Locate every blood parasite and identify its species.
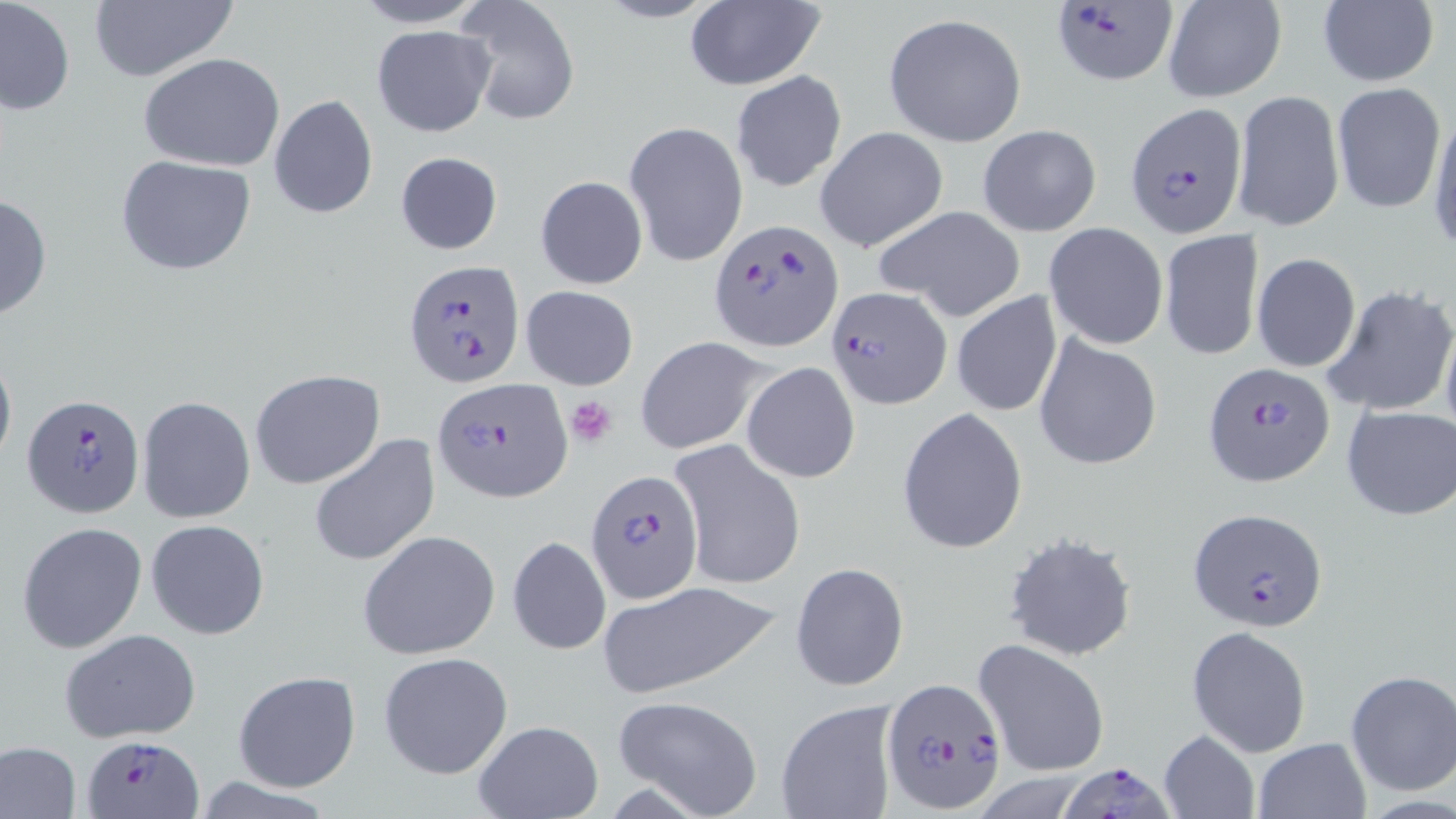

Approximate bounding boxes as named x1/y1/x2/y2 corners in pixels.
Plasmodium falciparum-infected red blood cells: (x1=1049, y1=0, x2=1177, y2=85), (x1=1125, y1=102, x2=1246, y2=235), (x1=711, y1=219, x2=841, y2=353), (x1=405, y1=259, x2=523, y2=389), (x1=826, y1=286, x2=951, y2=410), (x1=1200, y1=363, x2=1334, y2=488), (x1=433, y1=376, x2=571, y2=502), (x1=23, y1=393, x2=144, y2=518), (x1=585, y1=471, x2=703, y2=604), (x1=1188, y1=505, x2=1327, y2=633), (x1=881, y1=676, x2=1008, y2=814), (x1=78, y1=734, x2=207, y2=817), (x1=1057, y1=763, x2=1173, y2=819).
No Plasmodium ovale, Plasmodium malariae, Plasmodium vivax, Babesia divergens, or Trypanosoma brucei observed.

slide-level diagnosis = Plasmodium falciparum
field of view = one of a larger specimen
image size = 1456×819 pixels
stain = May-Grünwald-Giemsa
uninfected red blood cell locations = approximate bounding boxes as named x1/y1/x2/y2 corners in pixels: (x1=1, y1=0, x2=75, y2=116), (x1=347, y1=0, x2=493, y2=28), (x1=590, y1=0, x2=727, y2=24), (x1=1317, y1=0, x2=1439, y2=88), (x1=456, y1=1, x2=580, y2=126), (x1=1161, y1=1, x2=1287, y2=103), (x1=683, y1=2, x2=824, y2=90), (x1=87, y1=3, x2=239, y2=82), (x1=882, y1=13, x2=1027, y2=146), (x1=371, y1=25, x2=496, y2=135), (x1=138, y1=54, x2=285, y2=172), (x1=729, y1=70, x2=848, y2=193), (x1=1332, y1=81, x2=1446, y2=213), (x1=1232, y1=88, x2=1345, y2=232), (x1=268, y1=94, x2=378, y2=220), (x1=1426, y1=108, x2=1456, y2=258), (x1=623, y1=121, x2=748, y2=268), (x1=977, y1=125, x2=1103, y2=236), (x1=814, y1=127, x2=948, y2=252), (x1=394, y1=151, x2=504, y2=255), (x1=114, y1=155, x2=259, y2=277), (x1=534, y1=174, x2=648, y2=289), (x1=0, y1=193, x2=52, y2=321), (x1=873, y1=203, x2=1027, y2=321), (x1=1044, y1=222, x2=1169, y2=350), (x1=1159, y1=231, x2=1263, y2=360), (x1=1251, y1=253, x2=1361, y2=372), (x1=1321, y1=282, x2=1456, y2=417), (x1=520, y1=285, x2=640, y2=391), (x1=950, y1=292, x2=1063, y2=418), (x1=1439, y1=317, x2=1456, y2=450), (x1=1034, y1=334, x2=1163, y2=469), (x1=635, y1=335, x2=770, y2=454), (x1=0, y1=345, x2=16, y2=473), (x1=740, y1=361, x2=861, y2=484), (x1=250, y1=369, x2=385, y2=489), (x1=137, y1=395, x2=255, y2=523), (x1=1341, y1=404, x2=1456, y2=522), (x1=897, y1=406, x2=1028, y2=554), (x1=308, y1=433, x2=439, y2=567), (x1=669, y1=440, x2=805, y2=590), (x1=146, y1=518, x2=270, y2=640), (x1=17, y1=521, x2=148, y2=653), (x1=358, y1=530, x2=501, y2=661), (x1=1003, y1=532, x2=1139, y2=662), (x1=507, y1=535, x2=610, y2=654), (x1=791, y1=562, x2=909, y2=690), (x1=598, y1=581, x2=781, y2=696), (x1=1187, y1=625, x2=1311, y2=756), (x1=60, y1=630, x2=203, y2=742), (x1=973, y1=638, x2=1110, y2=778), (x1=377, y1=651, x2=513, y2=780), (x1=1345, y1=670, x2=1456, y2=795), (x1=232, y1=671, x2=362, y2=793), (x1=611, y1=695, x2=765, y2=819), (x1=775, y1=698, x2=900, y2=819), (x1=471, y1=719, x2=603, y2=819), (x1=1158, y1=730, x2=1260, y2=819), (x1=1252, y1=736, x2=1373, y2=819), (x1=0, y1=741, x2=82, y2=818)
preparation = thin blood film
platelet locations = approximate bounding boxes as named x1/y1/x2/y2 corners in pixels: (x1=564, y1=394, x2=621, y2=447)
magnification = 1000x
modality = light microscopy